Give the location of every parasitized red blood cell.
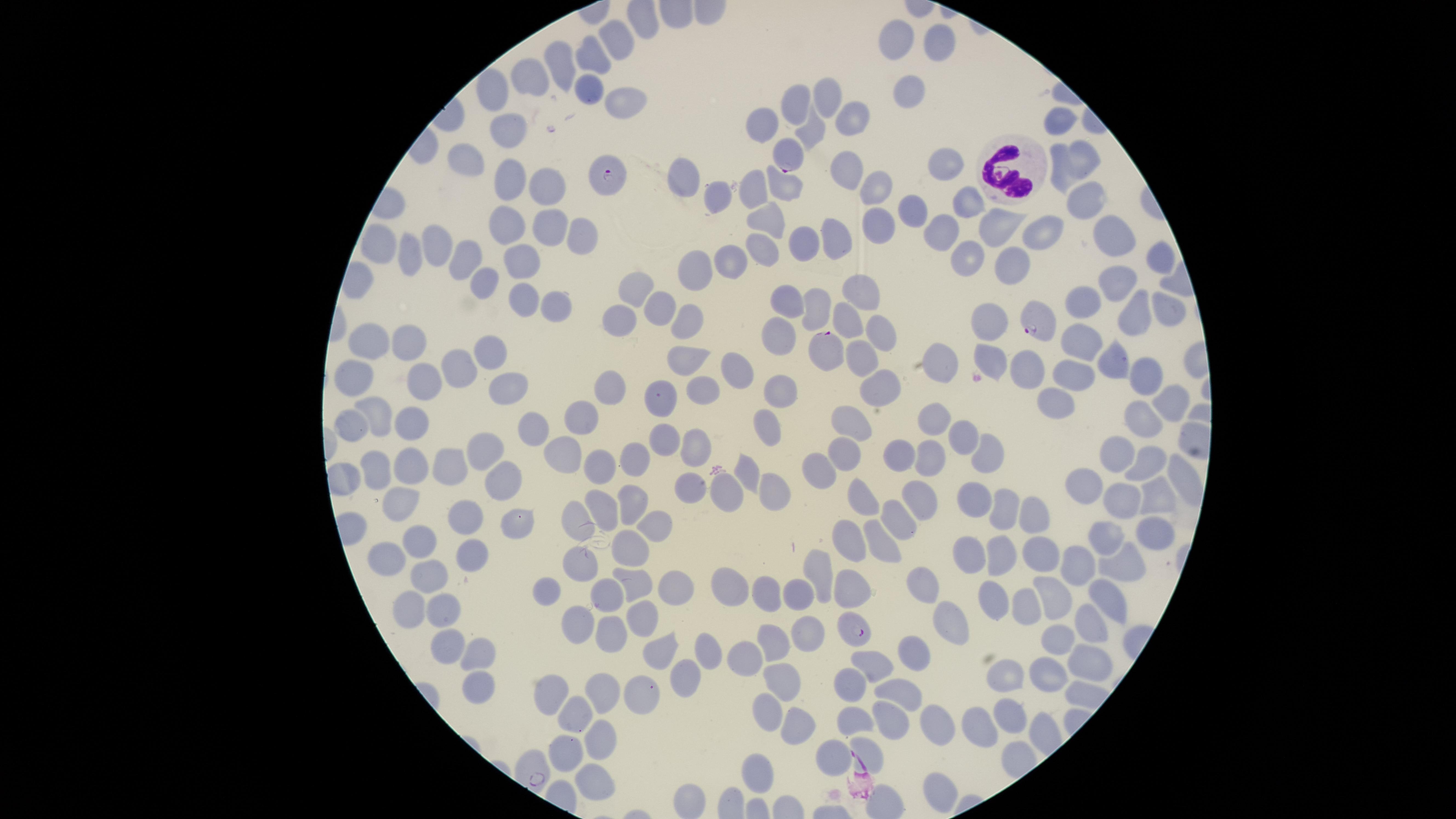
Approximate marker points as {x, y} in pixels.
Parasitized red blood cells: {787, 157}, {601, 174}, {1038, 325}, {831, 351}, {862, 630}.

preparation: thin blood smear
white_blood_cells: 'approximate marker points as {x, y} in pixels: {1014, 168}'
image_size: 1456×819 pixels
species: Plasmodium falciparum
stain: Giemsa
visible_region: circular
uninfected_red_blood_cells: 'approximate marker points as {x, y} in pixels: {898, 36}, {620, 37}, {936, 42}, {594, 56}, {562, 58}, {531, 80}, {494, 90}, {587, 90}, {912, 91}, {824, 97}, {614, 99}, {797, 103}, {853, 117}, {762, 122}, {1061, 122}, {511, 130}, {809, 133}, {466, 155}, {1079, 157}, {951, 164}, {845, 166}, {1062, 174}, {682, 175}, {504, 179}, {542, 181}, {783, 186}, {872, 189}, {722, 191}, {749, 192}, {1087, 197}, {966, 203}, {907, 210}, {769, 211}, {504, 223}, {882, 224}, {1004, 224}, {546, 227}, {942, 228}, {1052, 229}, {1108, 230}, {844, 232}, {575, 235}, {801, 243}, {763, 247}, {438, 248}, {379, 249}, {968, 254}, {409, 257}, {726, 259}, {1158, 259}, {525, 260}, {465, 261}, {1006, 261}, {696, 268}, {483, 281}, {1119, 284}, {630, 291}, {520, 297}, {859, 297}, {1088, 303}, {785, 307}, {813, 307}, {1168, 307}, {653, 308}, {547, 310}, {1137, 312}, {690, 317}, {841, 319}, {619, 320}, {993, 326}, {875, 327}, {774, 334}, {1081, 340}, {400, 343}, {369, 345}, {490, 351}, {1107, 354}, {866, 356}, {690, 357}, {992, 360}, {462, 366}, {1032, 368}, {1070, 371}, {738, 373}, {944, 373}, {355, 376}, {1146, 378}, {886, 379}, {422, 380}, {785, 386}, {511, 387}, {702, 389}, {609, 391}, {656, 398}, {1171, 401}, {1056, 406}, {936, 417}, {851, 418}, {1141, 419}, {375, 421}, {584, 423}, {414, 424}, {343, 427}, {767, 428}, {542, 430}, {667, 439}, {961, 442}, {697, 444}, {1117, 451}, {983, 452}, {487, 454}, {562, 454}, {845, 454}, {895, 454}, {633, 460}, {927, 460}, {405, 462}, {600, 463}, {1151, 465}, {450, 466}, {372, 469}, {817, 470}, {748, 471}, {1182, 473}, {1080, 480}, {501, 482}, {776, 484}, {722, 490}, {681, 492}, {1121, 495}, {859, 497}, {918, 497}, {402, 498}, {1156, 499}, {636, 501}, {979, 505}, {609, 508}, {1003, 511}, {516, 519}, {573, 520}, {902, 520}, {458, 521}, {1035, 522}, {656, 525}, {1151, 533}, {854, 535}, {1107, 538}, {879, 541}, {630, 545}, {420, 546}, {468, 550}, {385, 555}, {975, 555}, {1035, 556}, {1003, 559}, {1125, 560}, {583, 566}, {1080, 567}, {828, 569}, {429, 576}, {636, 580}, {674, 584}, {926, 585}, {857, 587}, {545, 588}, {731, 589}, {800, 590}, {605, 591}, {769, 594}, {1054, 595}, {1107, 595}, {999, 598}, {411, 603}, {446, 607}, {1028, 608}, {645, 619}, {951, 621}, {570, 622}, {1092, 624}, {604, 637}, {807, 641}, {444, 643}, {1062, 645}, {656, 649}, {777, 650}, {479, 651}, {705, 651}, {1092, 656}, {916, 657}, {750, 661}, {868, 663}, {683, 670}, {1013, 674}, {1046, 677}, {784, 680}, {478, 682}, {549, 686}, {845, 687}, {901, 692}, {603, 693}, {633, 695}, {1011, 711}, {756, 715}, {568, 716}, {854, 717}, {891, 721}, {793, 722}, {942, 727}, {981, 731}, {598, 741}, {867, 752}, {828, 755}, {568, 756}, {753, 769}, {592, 780}, {933, 786}, {693, 805}'
field_of_view: single
capture: smartphone photograph through the microscope eyepiece